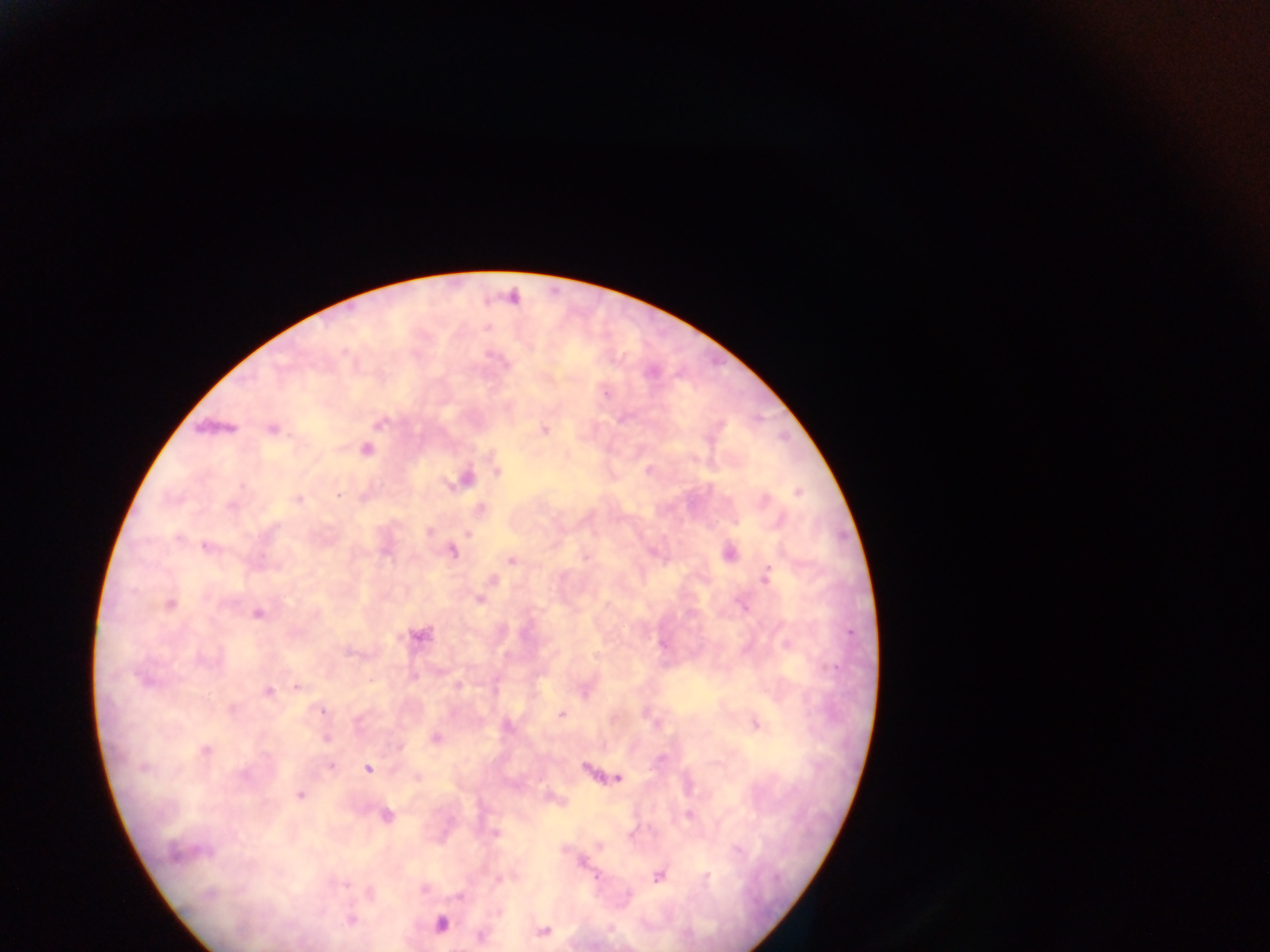

Approximate centers as {x, y} in pixels.
Summary:
  - Plasmodium parasite locations: {512, 297}, {606, 394}, {380, 423}, {272, 429}, {544, 431}, {366, 450}, {497, 471}, {465, 479}, {798, 492}, {339, 494}, {297, 499}, {231, 507}, {480, 509}, {429, 532}, {467, 533}, {178, 538}, {206, 547}, {452, 551}, {729, 554}, {587, 558}, {511, 561}, {767, 577}, {479, 601}, {170, 604}, {258, 613}, {420, 635}, {204, 661}, {146, 680}, {458, 685}, {298, 687}, {268, 691}, {232, 708}, {322, 712}, {561, 714}, {756, 724}, {435, 737}, {326, 738}, {400, 747}, {206, 750}, {331, 766}, {144, 768}, {368, 769}, {243, 776}, {417, 778}, {618, 779}, {300, 795}, {386, 815}, {689, 815}, {495, 833}, {205, 852}, {175, 853}, {582, 863}, {658, 876}, {707, 876}, {502, 879}, {346, 884}, {424, 889}, {208, 894}, {459, 896}, {350, 920}, {441, 924}, {543, 931}, {480, 937}
  - Capture: mobile-phone photograph through a microscope
  - Field of view: single
  - Country: Ghana
  - Image size: 1270×952 pixels
  - Preparation: thick blood smear